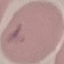

result = malaria parasites identified
stain = Giemsa
capture = smartphone camera at the microscope eyepiece
image type = automatically extracted cell patch, resized to 64 × 64 pixels
preparation = thin blood film